Classify this cell by malaria status.
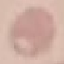

It is uninfected.

Thin smear of blood. Cell patch, automatically extracted from a larger field of view and resized to 64 × 64 pixels. Photographed with a smartphone camera at the microscope eyepiece. Giemsa-stained preparation.